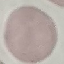

Result: no malaria parasites detected. Photographed with a smartphone camera at the microscope eyepiece. Cell patch, automatically extracted from a larger field of view and resized to 64 × 64 pixels. Thin smear of blood. Giemsa-stained preparation.